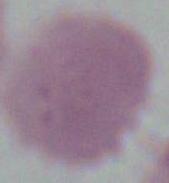 Captured at 1000x magnification. Micrograph. An erythrocyte is shown.